Classify this cell by malaria status.
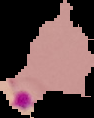

Parasitized.

image type = segmented cell region on a black background
image size = 94×118 pixels
preparation = thin blood smear